Classify this cell by malaria status.
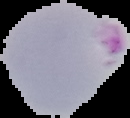

Parasitized.

image_type: segmented cell region on a black background
preparation: thin blood smear
image_size: 130×118 pixels